Assess this cell for malaria.
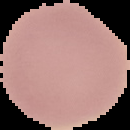

Uninfected.

The area outside the segmented cell region is set to black. Image is 130×130 pixels. From a thin blood film.